Identify the parasite.
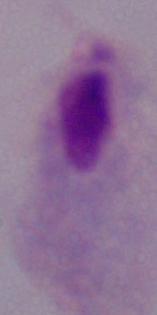
This is a trichomonad.

1000x magnification. Photomicrograph.